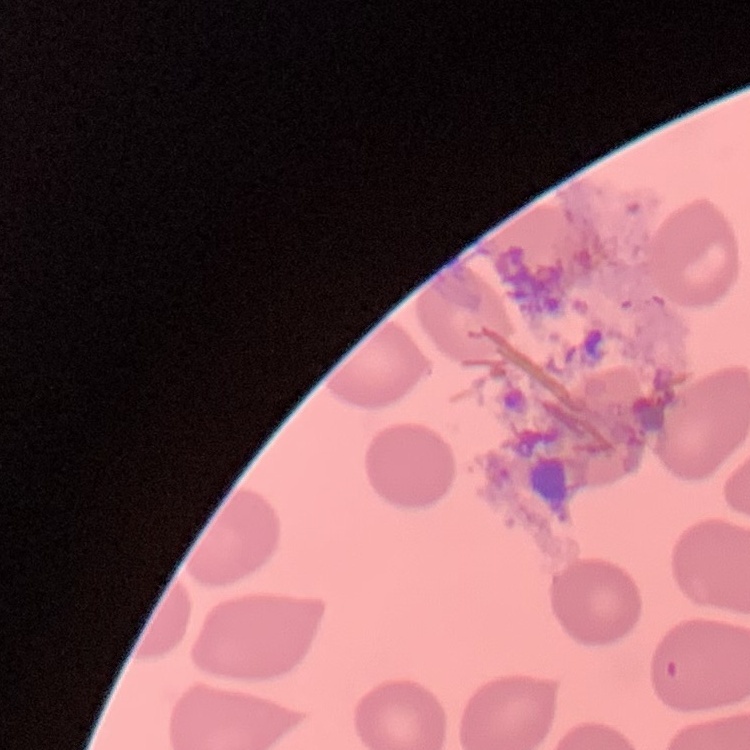

Summary:
  - Red blood cell morphology: no rouleaux formation
  - Preparation: thin blood smear
  - Stain: Field's or Giemsa
  - Image type: square crop of a larger photomicrograph